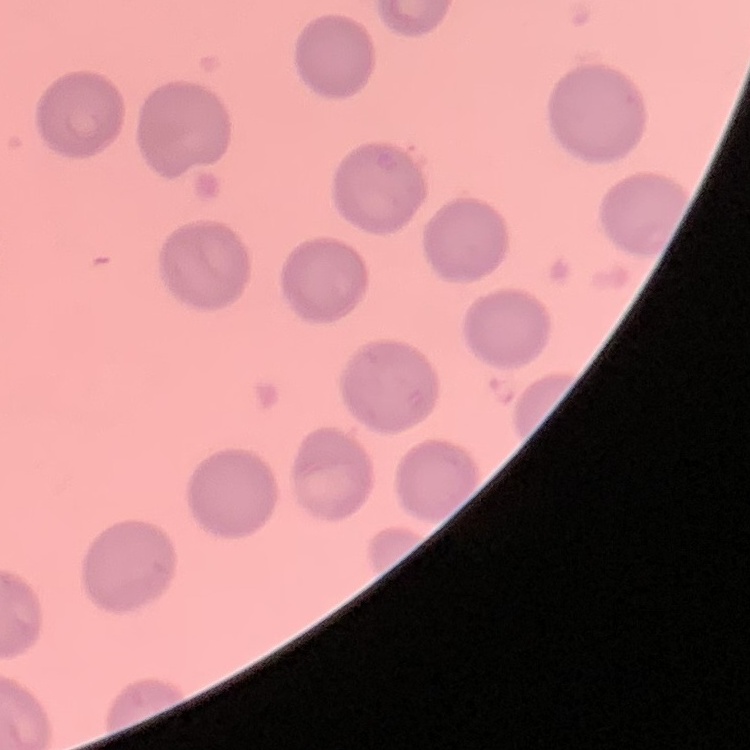
red_blood_cell_morphology: no rouleaux formation
preparation: thin blood smear
image_type: square crop of a larger photomicrograph
stain: Field's or Giemsa